Assess this cell for malaria.
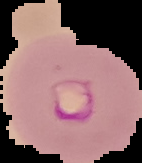
It is parasitized.

preparation = thin blood smear
image size = 142×163 pixels
image type = cell region segmented out of the field of view; surrounding area masked to black